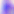

Summary:
  - Modality: micrograph
  - Magnification: 400x
  - Identification: Toxoplasma gondii